Give the extent of all Babesia divergens-infected red blood cells.
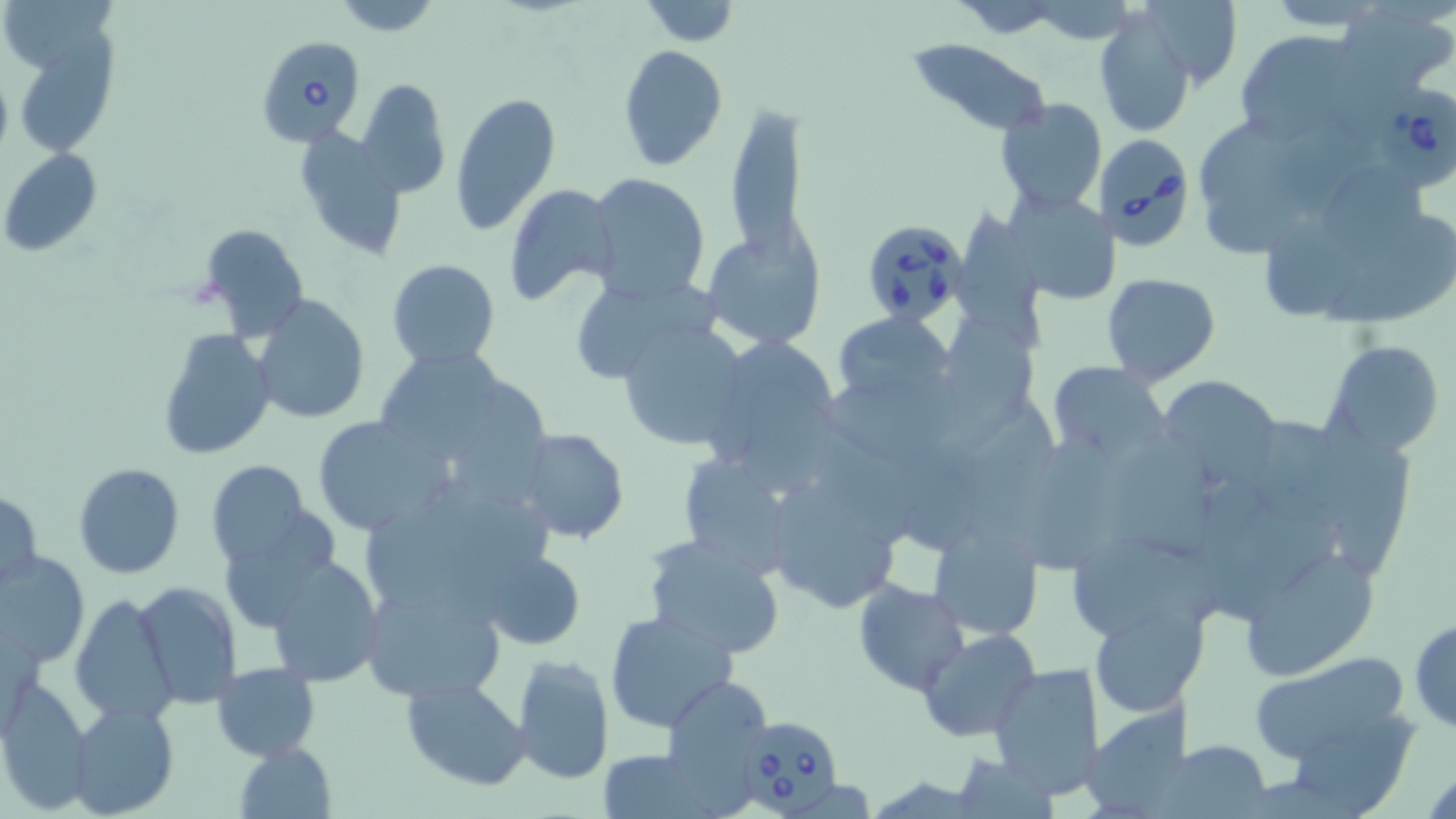

Approximate bounding boxes as [x1, y1, x2, y2] in pixels.
Babesia divergens-infected red blood cells: [256, 36, 367, 148], [1370, 87, 1456, 190], [1093, 133, 1196, 249], [862, 221, 972, 329], [740, 718, 849, 816].

Uninfected red blood cell locations: [333, 0, 440, 36], [639, 0, 741, 46], [1256, 0, 1399, 31], [949, 1, 1069, 35], [1139, 2, 1245, 93], [1336, 4, 1454, 98], [1095, 6, 1195, 137], [18, 30, 120, 153], [1233, 30, 1372, 149], [903, 36, 1054, 137], [618, 45, 728, 172], [356, 78, 451, 199], [449, 91, 561, 235], [992, 99, 1108, 215], [723, 103, 808, 268], [1201, 116, 1301, 209], [295, 129, 410, 261], [1, 148, 102, 256], [1330, 170, 1426, 252], [586, 172, 710, 303], [1206, 182, 1313, 258], [504, 183, 619, 306], [1009, 189, 1121, 304], [955, 206, 1046, 350], [1265, 211, 1370, 323], [1326, 217, 1456, 332], [199, 221, 311, 338], [704, 225, 825, 349], [386, 259, 501, 370], [1101, 272, 1219, 387], [578, 282, 724, 386], [252, 296, 371, 424], [832, 312, 956, 410], [949, 316, 1039, 451], [613, 319, 749, 452], [156, 328, 275, 460], [720, 331, 845, 487], [1324, 340, 1445, 457], [373, 347, 506, 464], [1048, 361, 1169, 461], [823, 372, 978, 472], [1157, 376, 1280, 488], [463, 380, 556, 506], [1255, 409, 1354, 525], [967, 413, 1065, 543], [312, 416, 451, 535], [1112, 425, 1213, 563], [815, 427, 917, 542], [517, 428, 629, 544], [1029, 428, 1127, 573], [1332, 436, 1414, 576], [896, 448, 994, 551], [670, 450, 803, 578], [206, 459, 314, 570], [73, 462, 185, 578], [762, 469, 910, 615], [435, 478, 566, 572], [1, 487, 43, 594], [227, 504, 344, 628], [368, 509, 473, 605], [927, 516, 1045, 640], [643, 533, 785, 658], [1063, 535, 1225, 632], [1233, 539, 1382, 682], [479, 548, 588, 650], [2, 550, 89, 668], [264, 556, 385, 688], [362, 578, 502, 702], [135, 580, 242, 708], [852, 581, 970, 697], [70, 593, 175, 725], [1088, 597, 1209, 716], [605, 610, 739, 734], [1409, 615, 1455, 734], [916, 628, 1041, 742], [1246, 651, 1414, 767], [511, 652, 615, 785], [988, 660, 1105, 800], [211, 662, 319, 762], [663, 674, 773, 799], [400, 677, 531, 789], [1, 679, 94, 815], [66, 699, 180, 818], [1083, 707, 1202, 815], [1160, 739, 1276, 817], [232, 741, 337, 818], [593, 748, 718, 817], [954, 750, 1056, 817]. Slide-level diagnosis: Babesia divergens. 1000x magnification. May-Grünwald-Giemsa-stained preparation. One field of a larger specimen. Optical microscopy. Thin blood smear. Image is 1456×819 pixels.